Assess for parasitized red blood cells.
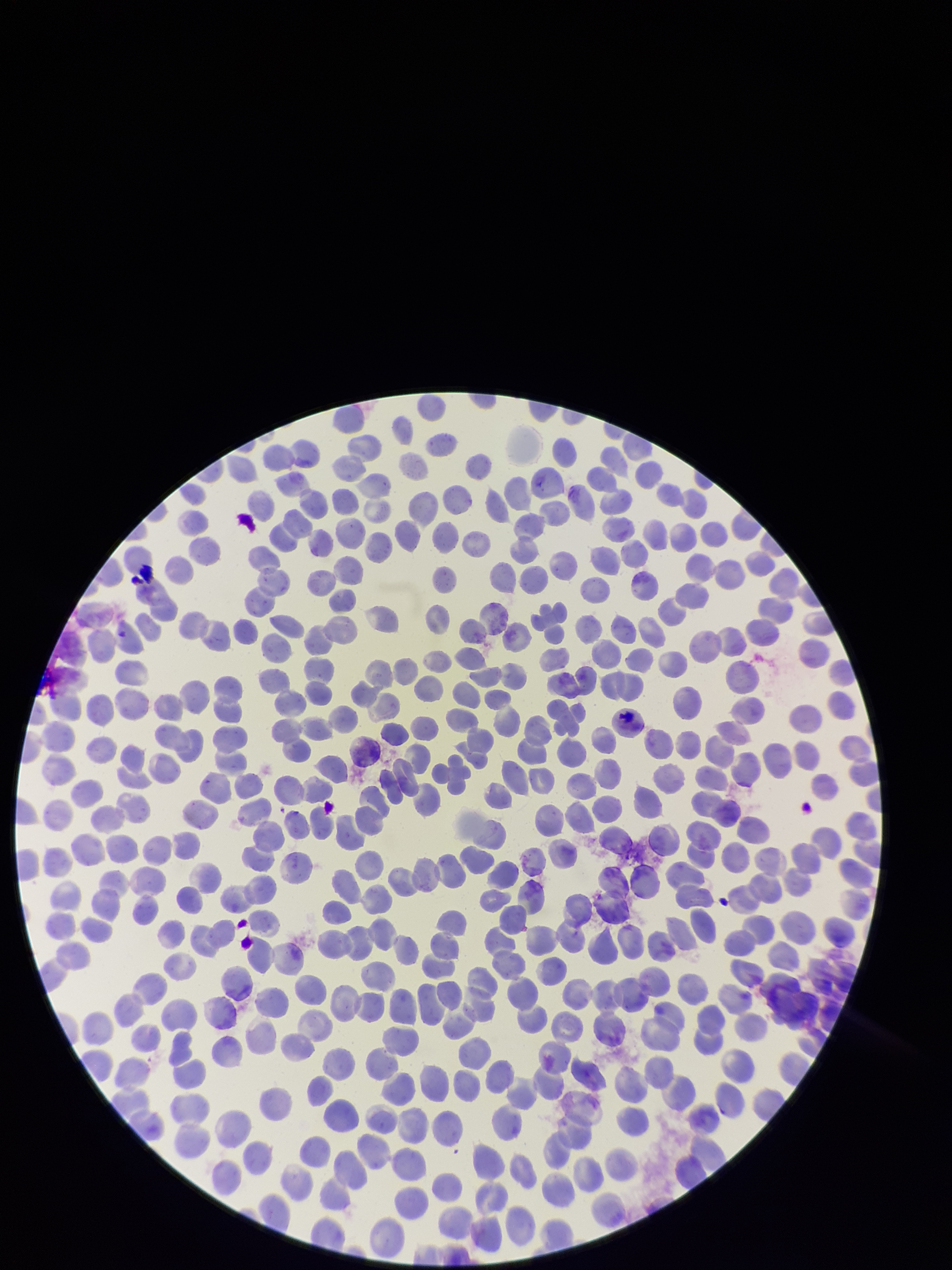

None detected.

Patient malaria status: negative. Red blood cell count: 239. Single field of view. Stained with Giemsa. Parasitized red blood cell count: 0. Preparation: thin blood smear. Image is 952×1270 pixels. Smartphone photograph taken through the eyepiece of a microscope.